Locate the cells, classifying each as a parasitized red blood cell, an uninfected red blood cell, or a white blood cell.
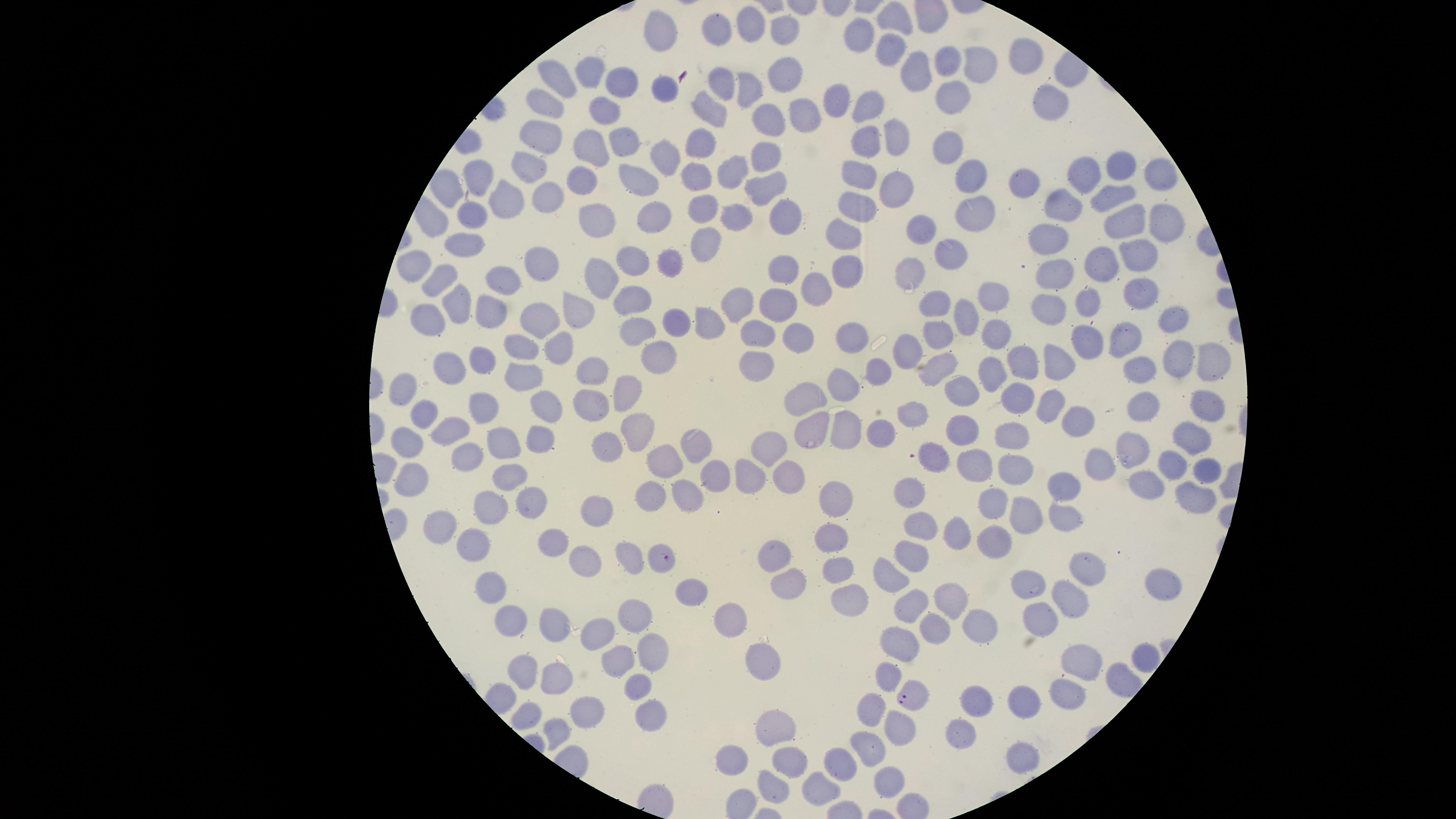
Approximate marker points as {x, y} in pixels.
Parasitized red blood cells: {662, 559}, {915, 697}.
Uninfected red blood cells: {754, 23}, {898, 23}, {785, 27}, {660, 28}, {719, 28}, {856, 37}, {893, 52}, {1024, 53}, {949, 56}, {981, 65}, {594, 69}, {921, 72}, {780, 73}, {560, 75}, {724, 80}, {749, 83}, {622, 85}, {668, 87}, {950, 92}, {839, 97}, {1044, 99}, {548, 104}, {710, 107}, {871, 110}, {605, 111}, {805, 111}, {769, 124}, {544, 131}, {899, 137}, {626, 140}, {871, 140}, {598, 147}, {702, 148}, {768, 149}, {946, 149}, {666, 156}, {1120, 165}, {1086, 171}, {735, 172}, {531, 173}, {1158, 175}, {976, 176}, {696, 177}, {860, 177}, {587, 178}, {1026, 180}, {640, 181}, {480, 182}, {763, 185}, {546, 190}, {893, 194}, {1113, 195}, {507, 198}, {1069, 202}, {706, 207}, {858, 207}, {473, 211}, {984, 215}, {736, 216}, {598, 219}, {657, 219}, {1165, 219}, {785, 220}, {1123, 222}, {923, 231}, {848, 235}, {1054, 240}, {705, 243}, {464, 246}, {948, 252}, {668, 258}, {1131, 259}, {636, 260}, {545, 261}, {1099, 263}, {421, 265}, {786, 265}, {852, 269}, {903, 269}, {1049, 275}, {604, 277}, {436, 281}, {504, 281}, {993, 286}, {819, 290}, {1146, 296}, {779, 297}, {630, 301}, {935, 301}, {452, 302}, {1049, 302}, {1092, 302}, {739, 303}, {490, 313}, {580, 315}, {434, 316}, {968, 316}, {1171, 318}, {672, 319}, {531, 322}, {704, 323}, {640, 328}, {939, 332}, {994, 334}, {801, 336}, {1123, 338}, {753, 340}, {1089, 340}, {853, 341}, {910, 343}, {517, 346}, {556, 350}, {481, 356}, {1213, 357}, {652, 358}, {1053, 358}, {1181, 360}, {1019, 361}, {942, 363}, {445, 365}, {594, 366}, {883, 367}, {753, 370}, {1139, 371}, {985, 377}, {523, 380}, {846, 382}, {410, 385}, {963, 387}, {623, 388}, {1013, 396}, {811, 400}, {1201, 400}, {590, 402}, {545, 403}, {485, 404}, {1056, 405}, {1148, 405}, {911, 409}, {421, 410}, {1081, 416}, {844, 428}, {812, 429}, {963, 430}, {880, 432}, {1006, 433}, {450, 436}, {634, 436}, {1189, 438}, {539, 439}, {411, 443}, {497, 444}, {690, 447}, {774, 447}, {1125, 450}, {606, 453}, {939, 459}, {467, 460}, {1175, 461}, {664, 462}, {1014, 463}, {1206, 463}, {1099, 464}, {980, 467}, {793, 474}, {756, 475}, {505, 477}, {713, 477}, {419, 479}, {1067, 481}, {1147, 485}, {1195, 485}, {912, 493}, {652, 494}, {689, 495}, {836, 497}, {526, 498}, {992, 503}, {490, 508}, {598, 510}, {1030, 515}, {1061, 518}, {918, 523}, {439, 524}, {959, 533}, {991, 536}, {831, 537}, {473, 545}, {551, 548}, {913, 553}, {774, 555}, {628, 559}, {587, 562}, {1081, 563}, {840, 566}, {890, 579}, {1027, 580}, {791, 582}, {1151, 588}, {690, 591}, {489, 592}, {948, 595}, {846, 598}, {919, 602}, {1065, 603}, {639, 613}, {1034, 618}, {512, 620}, {552, 620}, {982, 620}, {730, 621}, {935, 631}, {598, 636}, {903, 643}, {656, 653}, {1140, 654}, {764, 657}, {1084, 659}, {526, 663}, {621, 663}, {560, 668}, {892, 674}, {641, 689}, {1068, 689}, {1025, 699}, {979, 703}, {584, 707}, {872, 711}, {526, 713}, {649, 717}, {778, 721}, {905, 722}, {560, 729}, {961, 735}, {870, 739}, {1021, 755}, {728, 758}, {795, 761}, {843, 761}, {882, 781}, {772, 785}, {824, 792}.
No white blood cells identified.

Image is 1456×819 pixels. Thin blood smear. Photographed with a smartphone camera through the microscope eyepiece. One field of view of the specimen. The visible region is circular. Giemsa-stained preparation. Species: Plasmodium falciparum.